Assess this cell for malaria.
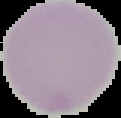
Uninfected.

Summary:
  - Image size: 121×118 pixels
  - Preparation: thin blood film
  - Image type: segmented cell region with the area outside set to black